Describe the morphology of the erythrocytes.
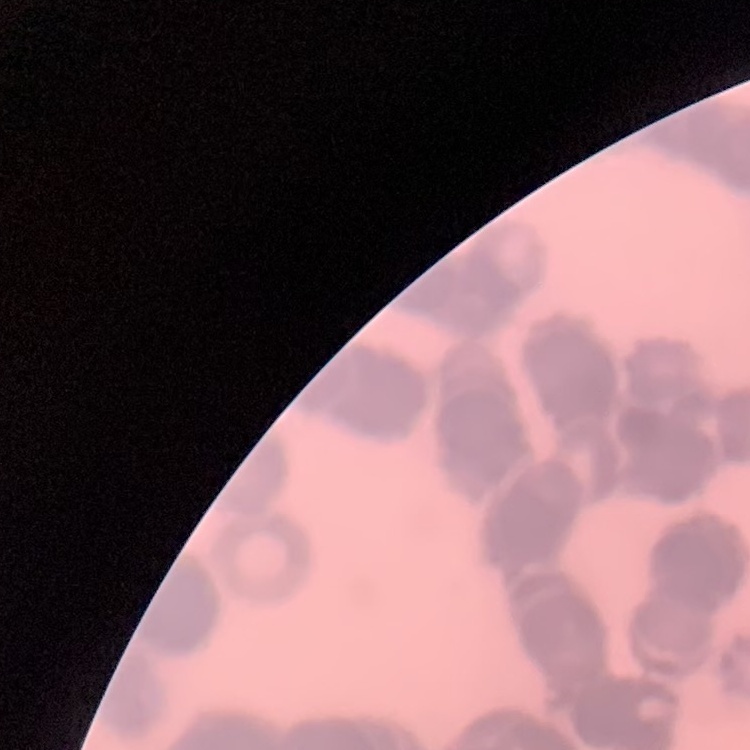

They show rouleaux formation.

Square crop of a larger photomicrograph. Field's or Giemsa stain. Thin peripheral smear.